Identify the cell.
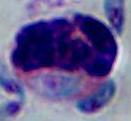
A leukocyte.

modality: micrograph
magnification: 1000x